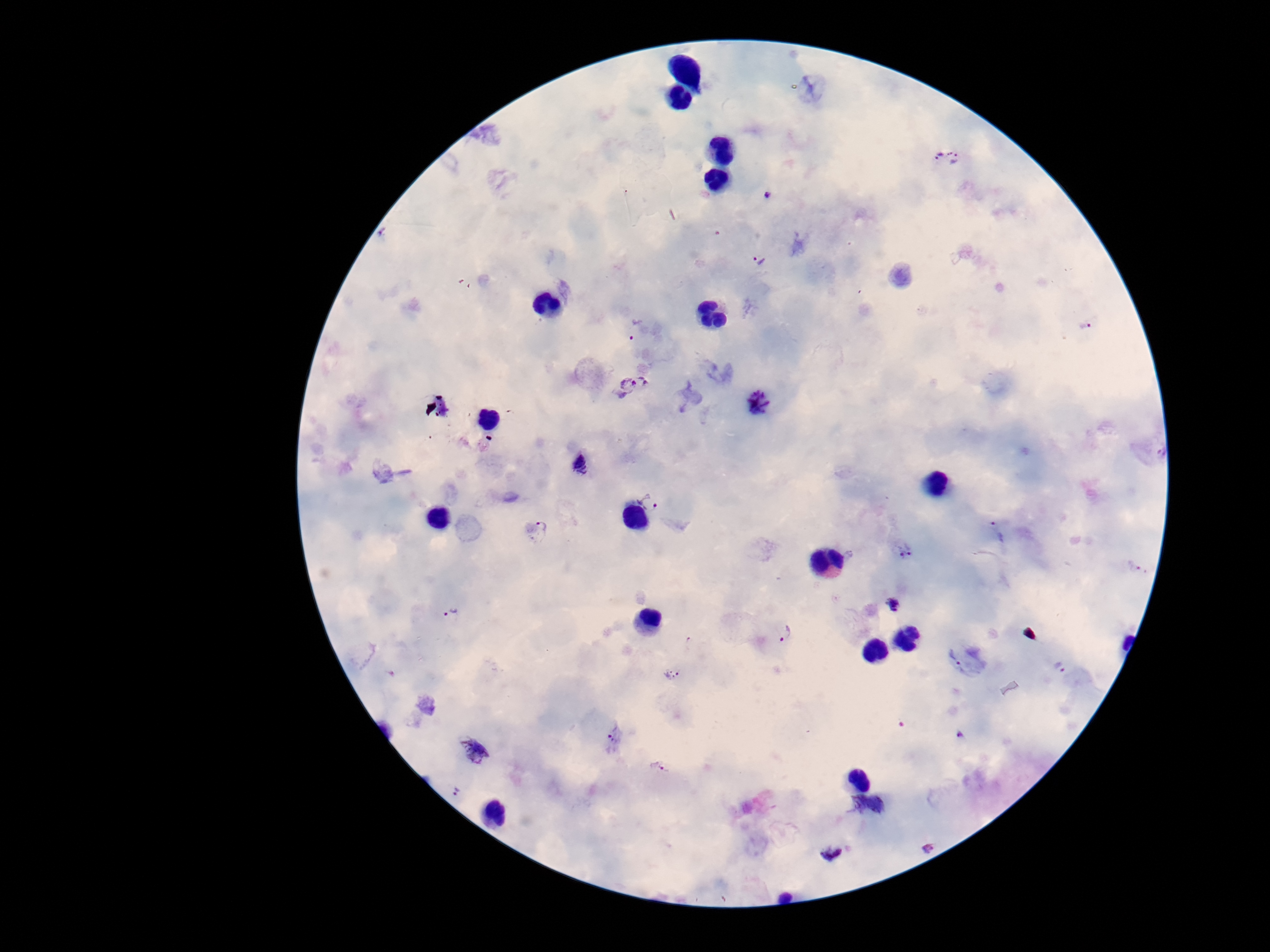 Approximate centers as (x, y) in pixels. Plasmodium parasite locations: (948, 157), (766, 196), (760, 262), (1085, 325), (637, 329), (632, 385), (760, 402), (1156, 451), (580, 464), (649, 503), (536, 531), (998, 531), (904, 551), (1136, 566), (894, 605), (451, 612), (782, 634), (967, 661), (1060, 667), (673, 674), (960, 734), (616, 738), (476, 751), (658, 767), (456, 794), (867, 804), (929, 848), (832, 852). 100x magnification. One field from this slide. Giemsa-stained preparation. Smartphone photograph taken through the microscope eyepiece. Image is 1270×952 pixels. Thick peripheral-blood smear. Patient malaria status: infected.